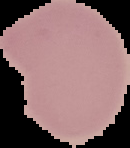
Summary:
  - Malaria status: uninfected
  - Preparation: thin blood film
  - Image type: segmented cell region with the area outside set to black
  - Image size: 130×148 pixels